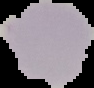
Summary:
  - Preparation: thin blood film
  - Image size: 94×88 pixels
  - Image type: segmented cell region on a black background
  - Malaria status: uninfected